Report the malaria status of this cell.
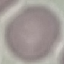

It is uninfected.

{
  "preparation": "thin blood film",
  "capture": "smartphone camera at the microscope eyepiece",
  "image_type": "cell patch, automatically extracted from a larger field of view and resized to 64 × 64 pixels",
  "stain": "Giemsa"
}